Identify the blood parasite species.
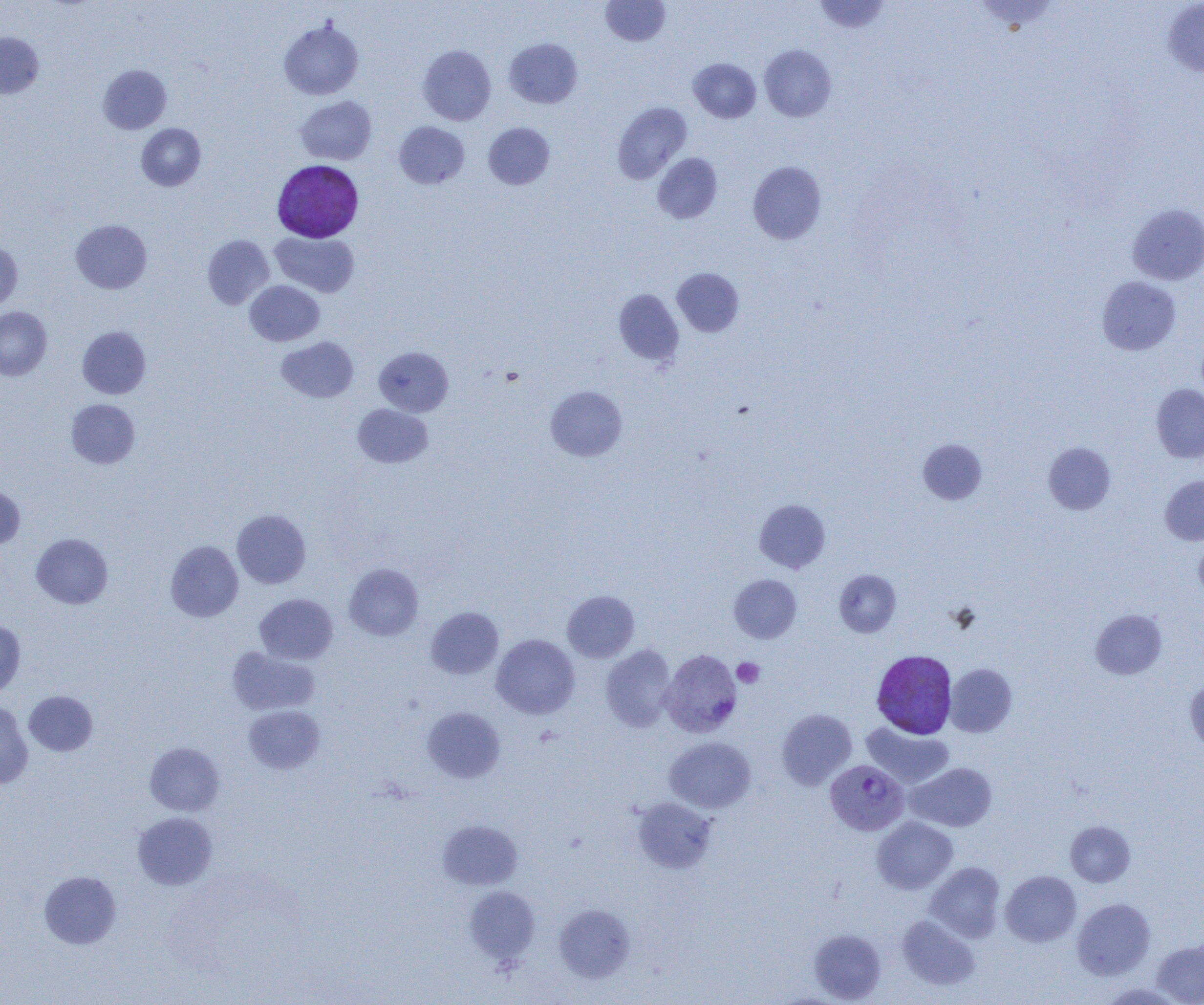
Plasmodium vivax.

Approximate bounding boxes as [x1, y1, x2, y2] in pixels. Plasmodium vivax-infected red blood cell locations: [271, 160, 363, 241], [660, 649, 742, 738], [871, 650, 957, 739], [826, 760, 909, 835]. Uninfected red blood cell locations: [601, 0, 670, 46], [813, 0, 890, 34], [973, 1, 1061, 34], [1162, 1, 1204, 77], [279, 20, 364, 100], [0, 32, 43, 99], [504, 37, 583, 108], [417, 45, 496, 125], [759, 45, 837, 122], [688, 58, 761, 122], [98, 65, 171, 134], [295, 96, 376, 164], [612, 102, 692, 183], [394, 121, 469, 189], [483, 122, 555, 189], [136, 123, 206, 191], [652, 153, 723, 224], [748, 161, 827, 244], [1127, 203, 1204, 285], [71, 219, 152, 293], [271, 231, 359, 297], [203, 235, 274, 309], [0, 242, 23, 311], [671, 268, 743, 337], [1097, 276, 1181, 355], [245, 280, 324, 346], [613, 289, 684, 366], [0, 306, 51, 380], [77, 326, 151, 399], [276, 336, 359, 403], [374, 346, 453, 416], [1151, 383, 1204, 463], [545, 386, 627, 461], [66, 399, 140, 469], [353, 404, 433, 468], [917, 438, 988, 505], [1043, 442, 1116, 514], [1160, 475, 1204, 545], [0, 486, 25, 549], [754, 499, 831, 573], [232, 509, 311, 589], [31, 533, 113, 609], [1194, 537, 1204, 602], [165, 540, 244, 622], [344, 563, 423, 641], [834, 570, 901, 637], [729, 574, 802, 643], [562, 590, 639, 662], [255, 593, 338, 664], [426, 607, 503, 679], [1090, 609, 1167, 679], [0, 618, 26, 696], [491, 635, 579, 719], [601, 644, 676, 731], [227, 646, 320, 716], [945, 664, 1017, 737], [1185, 677, 1204, 754], [24, 691, 98, 756], [0, 700, 33, 789], [243, 705, 325, 774], [422, 707, 505, 783], [776, 709, 857, 789], [861, 722, 953, 790], [664, 737, 756, 813], [145, 742, 225, 816], [906, 762, 997, 832], [631, 797, 717, 873], [132, 812, 217, 890], [872, 817, 958, 894], [437, 820, 523, 890], [1065, 821, 1135, 887], [925, 862, 1005, 942], [39, 870, 122, 949], [1001, 870, 1081, 946], [464, 886, 540, 964], [1072, 898, 1155, 980], [554, 903, 635, 982], [897, 915, 980, 991], [808, 929, 886, 1003], [1152, 938, 1204, 1004]. Platelet locations: [732, 658, 765, 688]. Light microscopy. Captured at 1000x magnification. Image is 1204×1005 pixels. Thin blood smear. One field of a larger specimen.